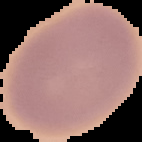

malaria status = uninfected
image size = 142×142 pixels
preparation = thin blood smear
image type = cell region segmented out of the field of view; surrounding area masked to black